Name the blood parasite species.
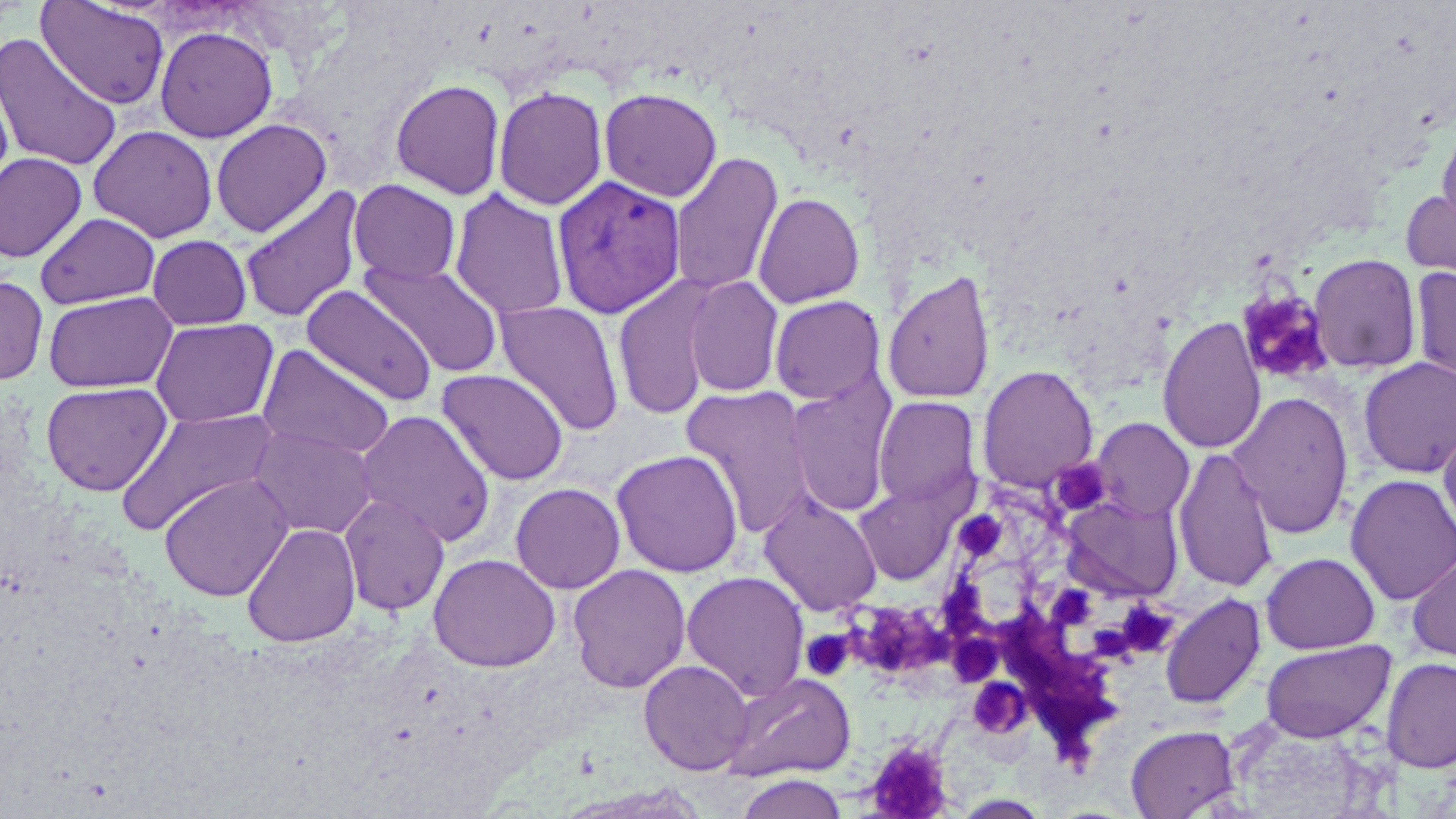

Plasmodium vivax.

platelet_locations: 'approximate bounding boxes as (x1, y1, x2, y2) in pixels: (1237, 289, 1334, 384), (1055, 459, 1107, 515), (956, 510, 1008, 564), (936, 581, 989, 633), (989, 590, 1119, 762), (1118, 603, 1179, 656), (862, 605, 953, 679), (944, 625, 1008, 679), (801, 630, 853, 680), (972, 675, 1030, 741), (864, 738, 956, 818)'
plasmodium_vivax_infected_red_blood_cell_locations: 'approximate bounding boxes as (x1, y1, x2, y2) in pixels: (552, 175, 686, 319)'
preparation: thin blood film
field_of_view: one of a larger specimen
uninfected_red_blood_cell_locations: 'approximate bounding boxes as (x1, y1, x2, y2) in pixels: (37, 0, 170, 109), (155, 26, 278, 143), (0, 32, 122, 171), (0, 73, 14, 200), (390, 79, 506, 200), (493, 86, 608, 211), (599, 87, 723, 202), (210, 118, 332, 237), (1436, 120, 1456, 238), (88, 124, 218, 242), (0, 152, 87, 263), (669, 152, 783, 296), (348, 179, 461, 285), (1400, 184, 1456, 293), (238, 185, 366, 326), (449, 188, 570, 320), (753, 191, 865, 308), (35, 212, 160, 309), (146, 234, 252, 330), (1307, 253, 1422, 373), (362, 260, 504, 378), (1410, 265, 1456, 391), (882, 269, 996, 405), (0, 275, 48, 385), (612, 275, 720, 421), (683, 276, 785, 398), (301, 285, 437, 407), (43, 290, 178, 393), (769, 295, 885, 404), (494, 301, 625, 436), (1157, 315, 1266, 455), (150, 317, 279, 428), (257, 345, 394, 462), (1358, 357, 1456, 478), (977, 365, 1098, 492), (436, 368, 570, 486), (785, 374, 898, 518), (40, 381, 173, 496), (679, 385, 817, 538), (1228, 391, 1354, 539), (873, 396, 981, 510), (116, 407, 279, 535), (355, 409, 497, 547), (1091, 417, 1195, 522), (1439, 419, 1456, 543), (248, 424, 378, 540), (1173, 446, 1280, 593), (611, 449, 743, 577), (160, 473, 294, 602), (1345, 474, 1456, 605), (853, 480, 963, 586), (510, 482, 626, 594), (758, 491, 883, 617), (339, 493, 450, 616), (1061, 493, 1184, 602), (241, 523, 361, 647), (1406, 549, 1456, 663), (1261, 552, 1379, 654), (427, 553, 561, 672), (567, 564, 691, 693), (681, 570, 810, 702), (1160, 593, 1266, 709), (1261, 639, 1395, 742), (1381, 657, 1456, 774), (638, 660, 754, 775), (722, 672, 855, 782), (1219, 715, 1391, 818), (1125, 724, 1240, 818), (735, 773, 850, 818)'
modality: optical microscopy
stain: May-Grünwald-Giemsa
image_size: 1456×819 pixels
magnification: 1000x